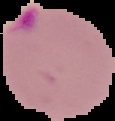 Malaria status: parasitized. From a thin blood smear. Segmented cell region on a black background. Image is 115×121 pixels.